Evaluate for malaria.
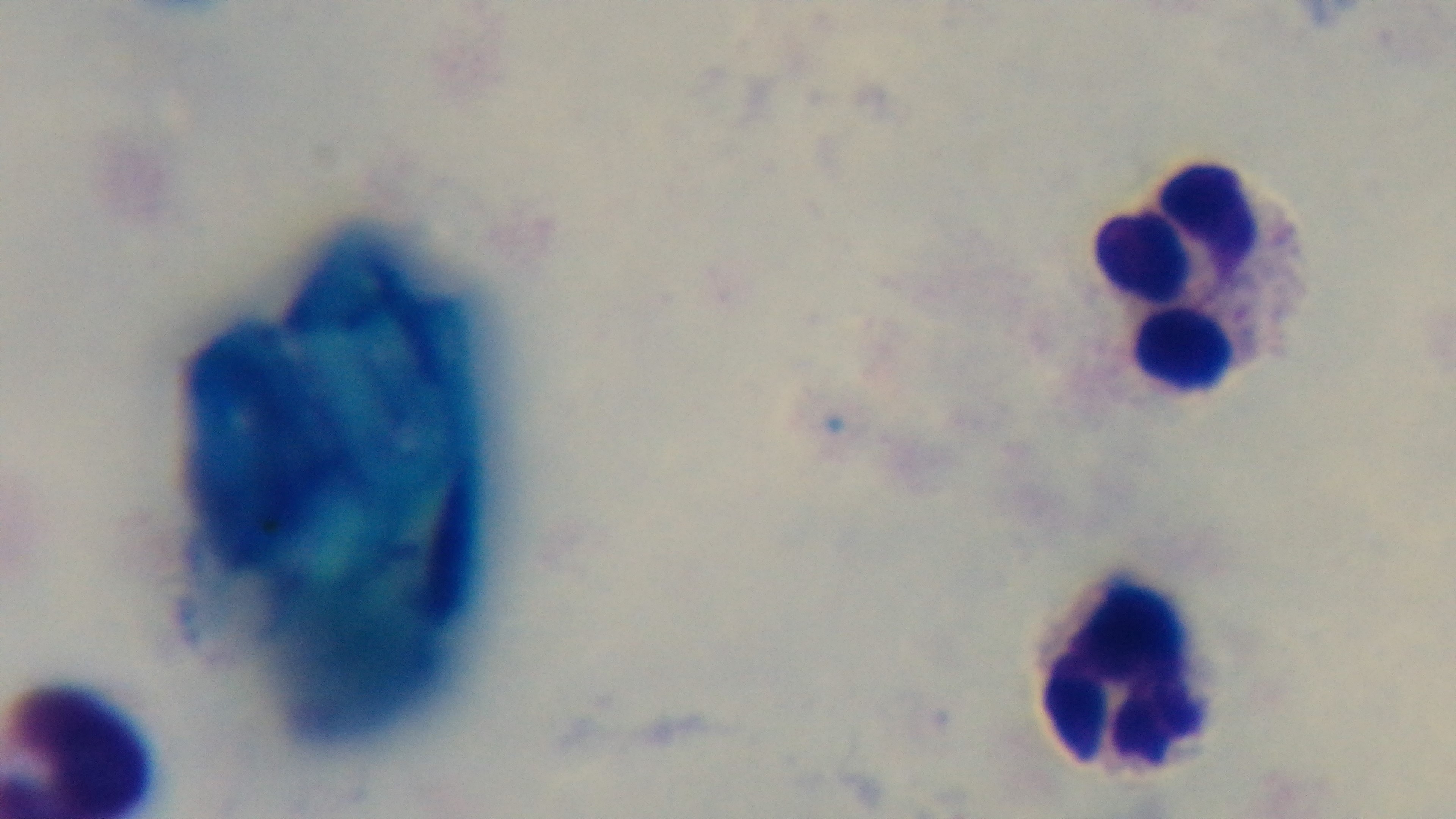

Uninfected.

modality = light microscopy
field of view = single
stain = Giemsa
capture = mounted 4K digital camera
objective = 100x oil immersion
preparation = thick smear